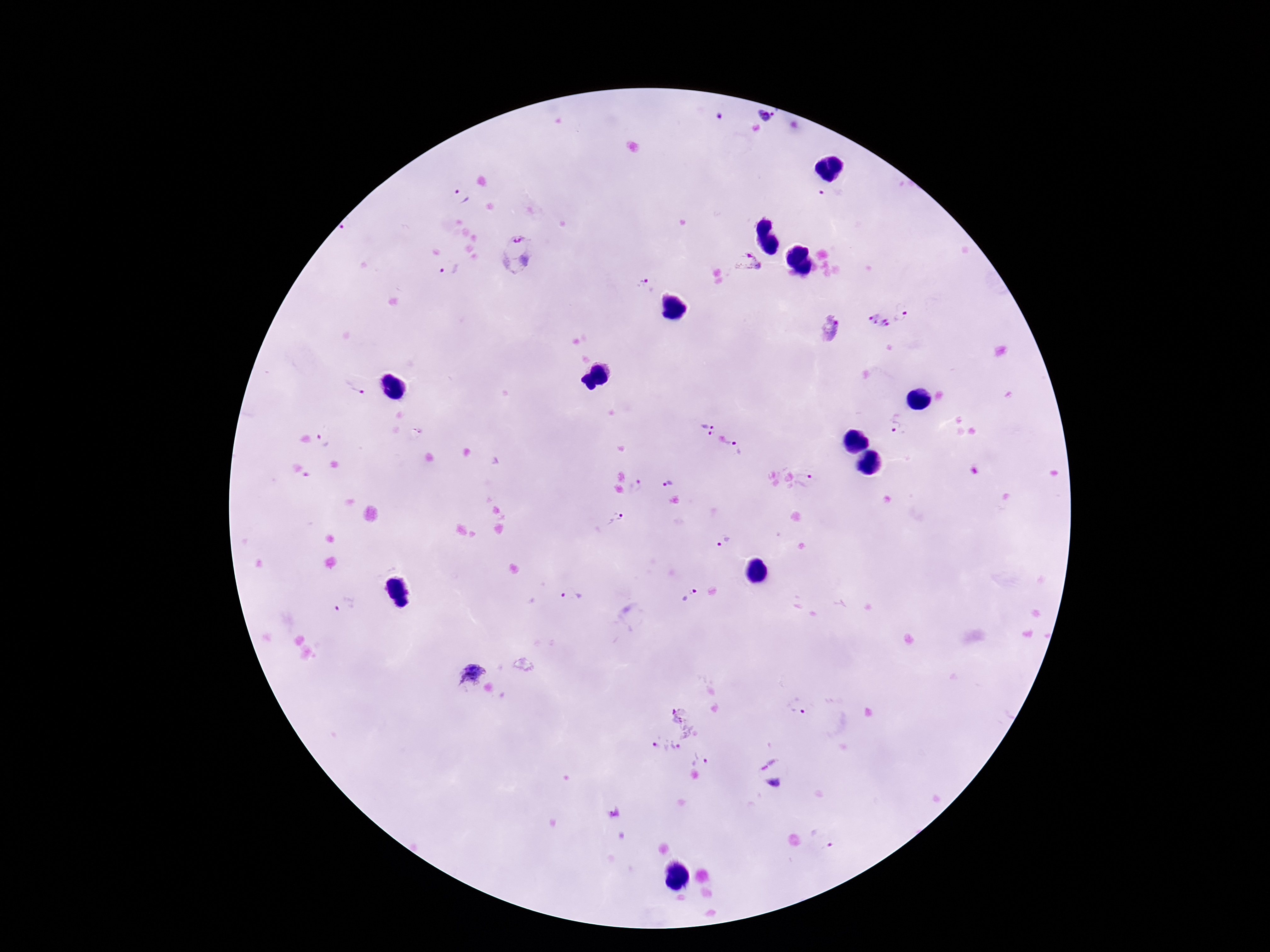
Approximate centers as (x, y) in pixels.
Summary:
  - Plasmodium parasite locations: (768, 114), (832, 195), (461, 197), (514, 253), (747, 261), (449, 270), (647, 286), (906, 311), (878, 323), (830, 331), (353, 385), (898, 426), (706, 428), (325, 440), (741, 448), (808, 479), (667, 483), (637, 486), (617, 518), (723, 540), (692, 592), (576, 594), (345, 606), (470, 675), (801, 705), (684, 719), (665, 749), (703, 758), (772, 772), (821, 838)
  - Field of view: single
  - Capture: smartphone camera through the microscope eyepiece
  - Preparation: thick blood smear
  - Stain: Giemsa
  - Patient malaria status: positive
  - Magnification: 100x
  - Image size: 1270×952 pixels